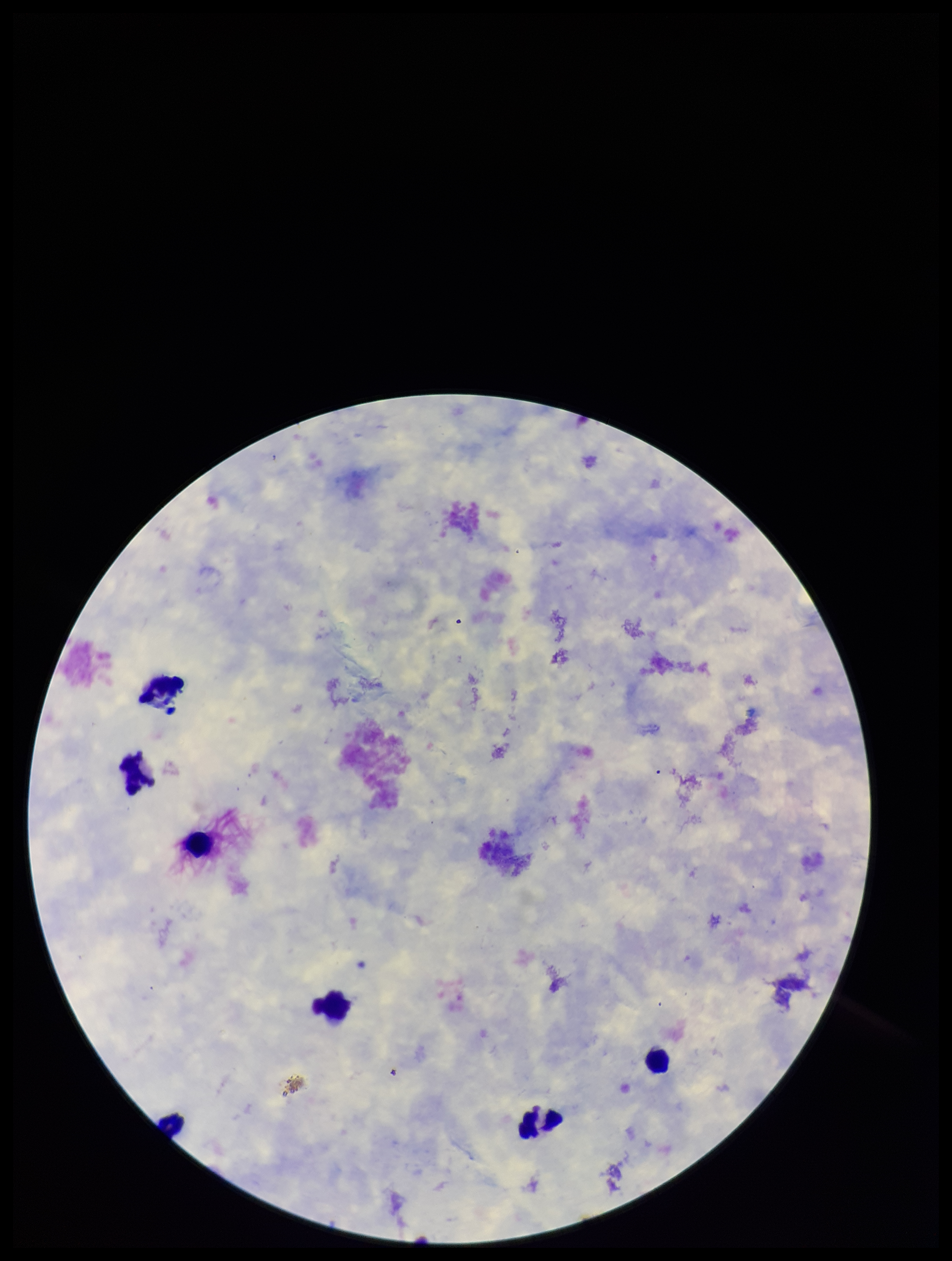

Summary:
  - Leukocyte count: 6
  - Parasite count: 0
  - Field of view: single
  - Image size: 952×1261 pixels
  - Capture: smartphone photograph through the microscope eyepiece
  - Plasmodium parasites: none identified
  - Preparation: thick smear
  - Stain: Giemsa
  - Patient malaria status: negative